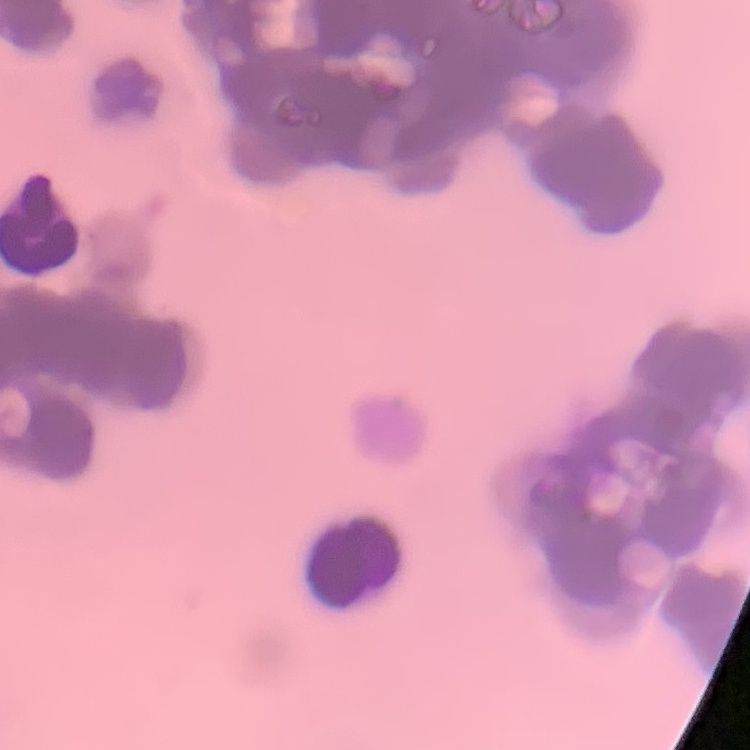
Summary:
  - Red blood cell morphology: rouleaux formation
  - Image type: one tile cut from a larger photomicrograph
  - Preparation: thin blood film
  - Stain: Field's or Giemsa